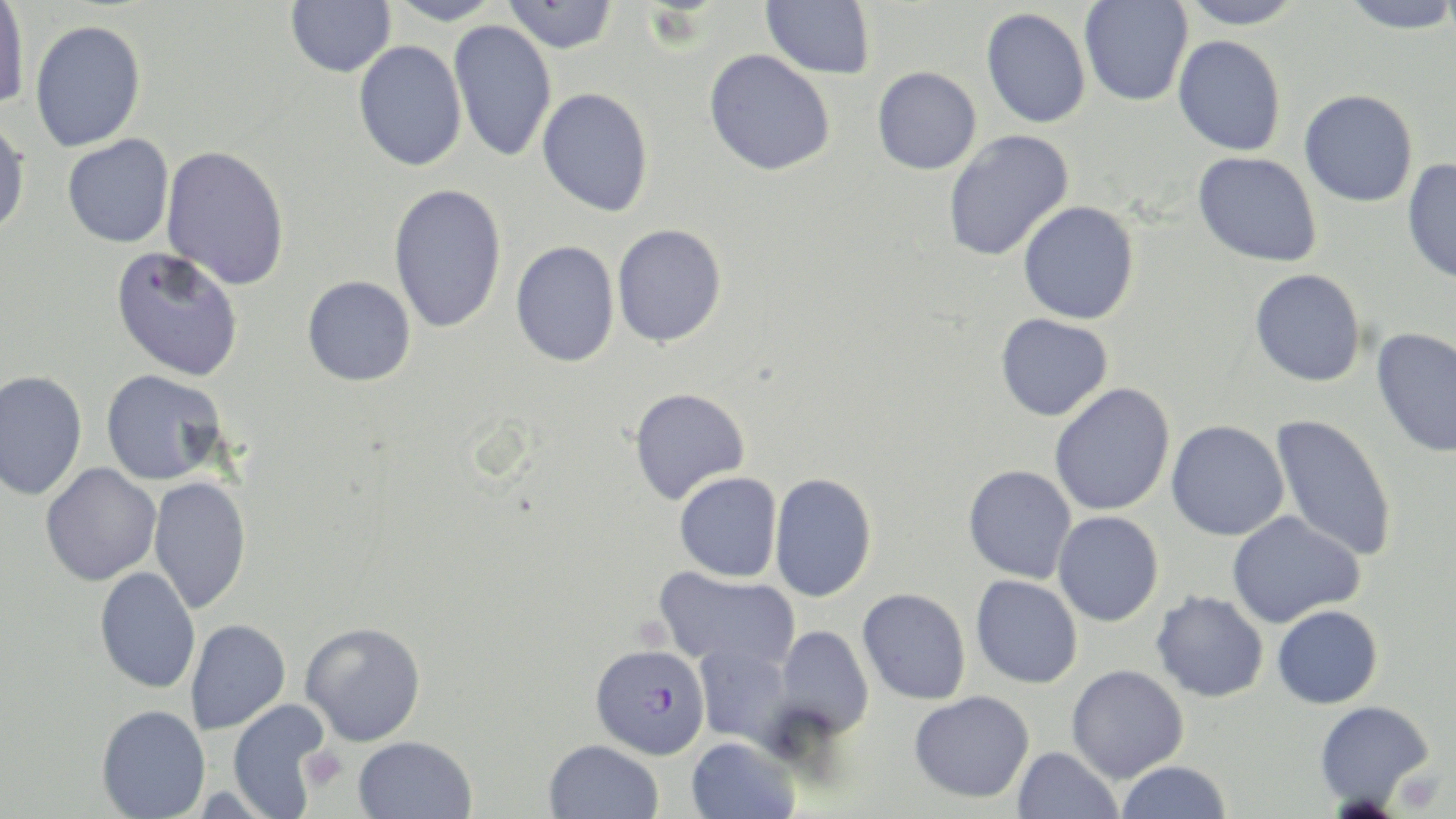

slide_level_diagnosis: Plasmodium falciparum
stain: May-Grünwald-Giemsa
plasmodium_falciparum_infected_red_blood_cell_locations: 'approximate bounding boxes as (x1,y1)-(x2,y2) corner pairs in pixels: (595,650)-(706,759)'
platelet_locations: 'approximate bounding boxes as (x1,y1)-(x2,y2) corner pairs in pixels: (302,747)-(349,791)'
preparation: thin blood smear
image_size: 1456×819 pixels
modality: light microscopy
magnification: 1000x
uninfected_red_blood_cell_locations: 'approximate bounding boxes as (x1,y1)-(x2,y2) corner pairs in pixels: (0,0)-(30,110), (285,0)-(396,77), (385,0)-(505,25), (502,0)-(618,54), (761,0)-(875,79), (1079,0)-(1193,106), (1176,0)-(1305,29), (1338,0)-(1456,33), (981,7)-(1091,128), (448,20)-(557,162), (29,21)-(146,152), (1173,35)-(1286,156), (353,40)-(467,171), (704,48)-(836,176), (872,66)-(981,174), (537,87)-(654,216), (1299,89)-(1418,207), (0,116)-(30,237), (942,129)-(1075,263), (62,134)-(174,248), (161,144)-(290,290), (1193,151)-(1322,267), (1401,158)-(1456,286), (388,182)-(507,334), (1017,201)-(1140,324), (612,224)-(727,347), (510,240)-(620,367), (110,246)-(245,381), (1249,268)-(1366,387), (302,275)-(416,386), (995,313)-(1113,421), (1371,327)-(1456,459), (100,369)-(229,485), (0,371)-(87,500), (1049,383)-(1175,517), (629,387)-(750,505), (1269,412)-(1397,563), (1165,420)-(1290,541), (40,463)-(161,586), (963,465)-(1077,584), (674,472)-(782,582), (769,472)-(877,602), (148,476)-(251,615), (1226,509)-(1367,628), (1053,511)-(1164,626), (94,567)-(201,693), (654,567)-(800,671), (970,575)-(1083,689), (857,588)-(971,705), (1150,589)-(1269,702), (1272,604)-(1383,709), (185,619)-(291,735), (300,621)-(427,746), (774,625)-(874,740), (693,643)-(795,749), (1066,664)-(1189,783), (909,690)-(1035,803), (227,699)-(330,818), (1314,700)-(1435,811), (96,704)-(210,819), (352,735)-(477,819), (686,736)-(799,819), (543,739)-(664,819), (1012,746)-(1124,819), (1116,760)-(1231,819)'
field_of_view: one of a larger specimen